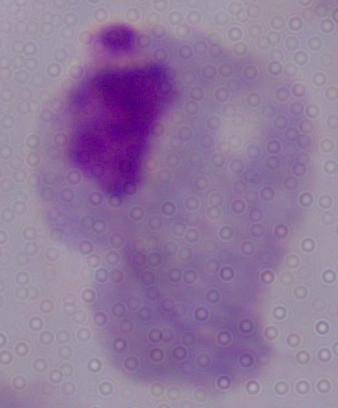

modality = micrograph
magnification = 1000x
identification = trichomonad